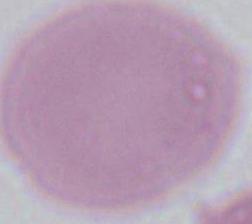
Summary:
  - Identification: red blood cell
  - Magnification: 1000x
  - Modality: photomicrograph